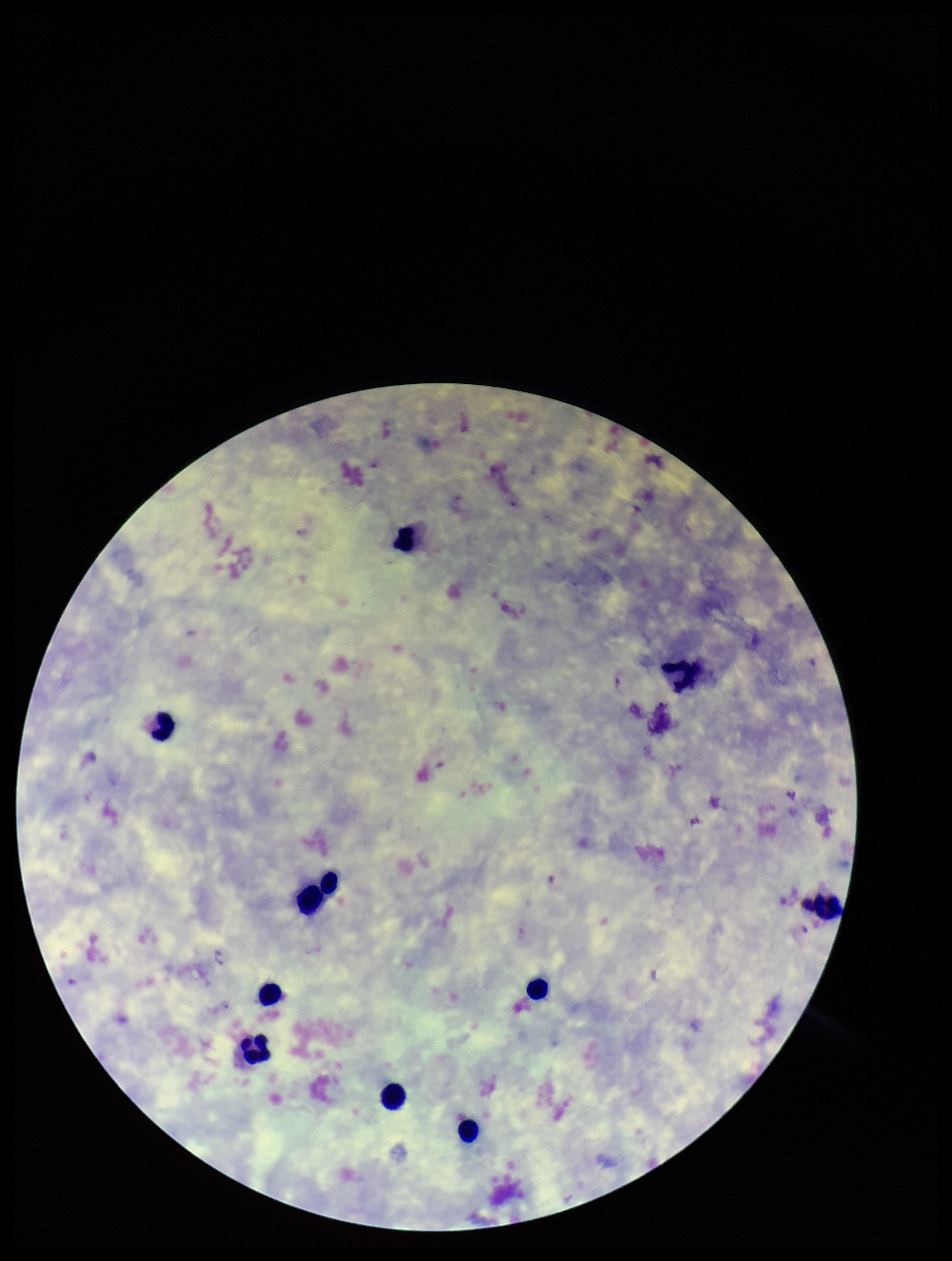
preparation = thick smear
Plasmodium parasites = detected
capture = smartphone photograph through the microscope eyepiece
stain = Giemsa
image size = 952×1261 pixels
species reported for this patient = Plasmodium vivax
leukocyte count = 11
parasite count = 1
patient malaria status = positive
field of view = single